Assess the morphology of the red blood cells.
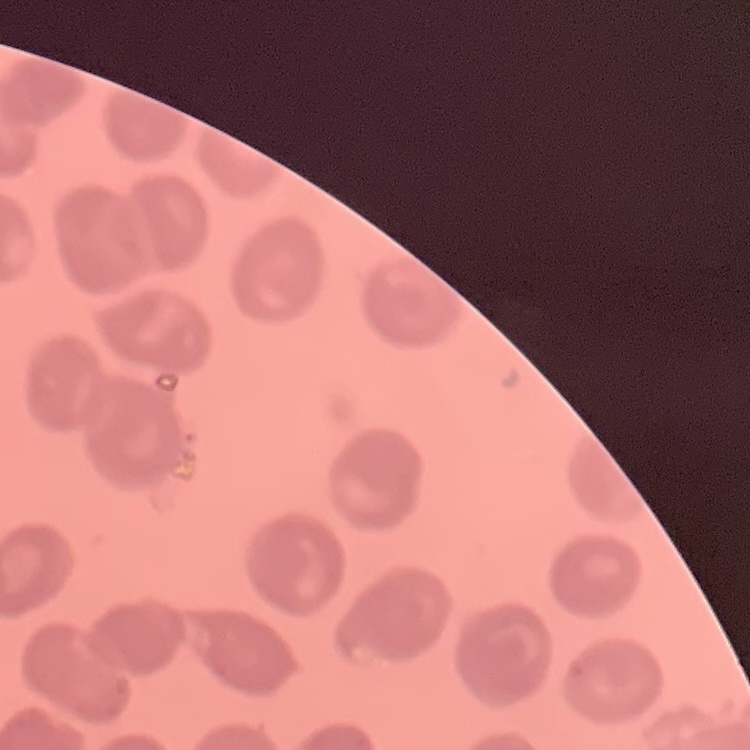
They show no rouleaux formation.

preparation = thin blood film
stain = Field's or Giemsa
image type = square crop of a larger photomicrograph